State the blood parasite species.
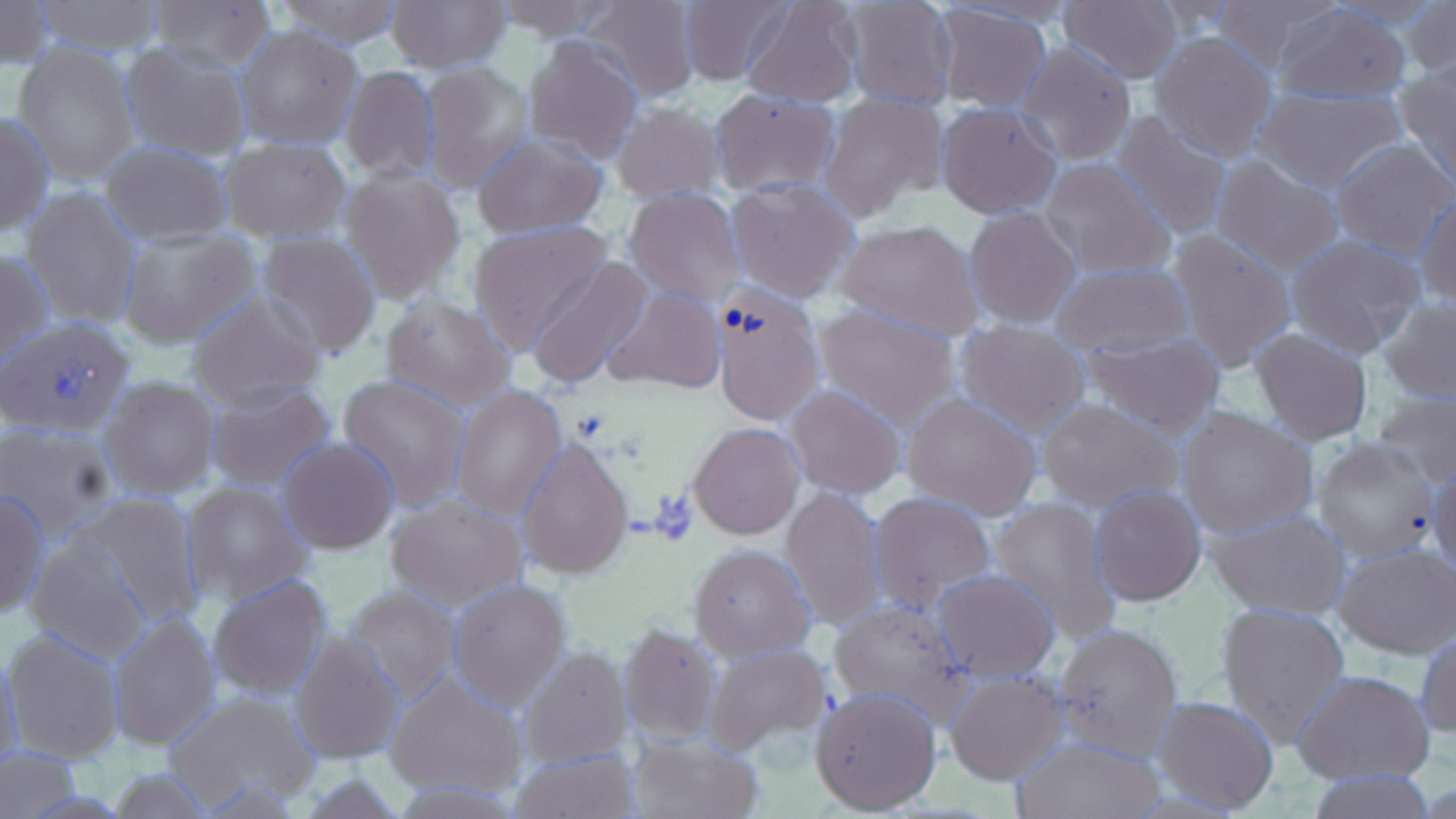
Plasmodium ovale.

Summary:
  - Coordinate format: approximate bounding boxes as named x1/y1/x2/y2 corners in pixels
  - Platelet locations: (x1=49, y1=357, x2=98, y2=403), (x1=649, y1=490, x2=699, y2=544)
  - Plasmodium ovale-infected red blood cell locations: (x1=710, y1=280, x2=825, y2=427)
  - Uninfected red blood cell locations: (x1=0, y1=0, x2=53, y2=71), (x1=32, y1=0, x2=166, y2=54), (x1=147, y1=0, x2=276, y2=71), (x1=271, y1=0, x2=408, y2=47), (x1=491, y1=0, x2=630, y2=42), (x1=680, y1=0, x2=798, y2=88), (x1=740, y1=0, x2=865, y2=108), (x1=840, y1=0, x2=958, y2=109), (x1=1058, y1=0, x2=1184, y2=83), (x1=1205, y1=0, x2=1347, y2=71), (x1=386, y1=1, x2=513, y2=73), (x1=578, y1=1, x2=697, y2=102), (x1=1405, y1=1, x2=1456, y2=89), (x1=931, y1=3, x2=1055, y2=115), (x1=1269, y1=3, x2=1412, y2=104), (x1=235, y1=25, x2=364, y2=149), (x1=1149, y1=32, x2=1277, y2=160), (x1=522, y1=36, x2=645, y2=163), (x1=120, y1=41, x2=252, y2=161), (x1=12, y1=42, x2=141, y2=187), (x1=1016, y1=42, x2=1135, y2=166), (x1=418, y1=62, x2=534, y2=191), (x1=1395, y1=62, x2=1456, y2=187), (x1=340, y1=65, x2=438, y2=182), (x1=1256, y1=84, x2=1404, y2=191), (x1=709, y1=87, x2=840, y2=197), (x1=821, y1=92, x2=946, y2=220), (x1=610, y1=102, x2=725, y2=202), (x1=937, y1=102, x2=1062, y2=218), (x1=0, y1=110, x2=53, y2=236), (x1=1113, y1=111, x2=1232, y2=238), (x1=470, y1=134, x2=608, y2=239), (x1=219, y1=136, x2=350, y2=242), (x1=1330, y1=139, x2=1456, y2=260), (x1=100, y1=143, x2=232, y2=244), (x1=1212, y1=155, x2=1345, y2=275), (x1=1039, y1=159, x2=1174, y2=278), (x1=341, y1=167, x2=467, y2=305), (x1=725, y1=177, x2=858, y2=301), (x1=21, y1=187, x2=142, y2=328), (x1=625, y1=187, x2=742, y2=307), (x1=1414, y1=196, x2=1456, y2=305), (x1=965, y1=206, x2=1081, y2=328), (x1=834, y1=219, x2=985, y2=340), (x1=468, y1=220, x2=614, y2=348), (x1=115, y1=227, x2=260, y2=349), (x1=1165, y1=228, x2=1298, y2=374), (x1=256, y1=232, x2=382, y2=357), (x1=1285, y1=233, x2=1425, y2=358), (x1=1, y1=248, x2=50, y2=373), (x1=529, y1=257, x2=654, y2=387), (x1=1052, y1=261, x2=1191, y2=358), (x1=603, y1=288, x2=724, y2=394), (x1=188, y1=291, x2=326, y2=410), (x1=380, y1=294, x2=515, y2=409), (x1=1376, y1=296, x2=1456, y2=404), (x1=812, y1=304, x2=960, y2=426), (x1=2, y1=317, x2=136, y2=438), (x1=956, y1=321, x2=1089, y2=434), (x1=1251, y1=327, x2=1374, y2=447), (x1=1081, y1=330, x2=1224, y2=438), (x1=338, y1=373, x2=471, y2=509), (x1=101, y1=376, x2=218, y2=498), (x1=205, y1=378, x2=337, y2=492), (x1=451, y1=384, x2=566, y2=522), (x1=787, y1=386, x2=906, y2=497), (x1=1370, y1=387, x2=1456, y2=489), (x1=901, y1=392, x2=1041, y2=521), (x1=1036, y1=399, x2=1184, y2=510), (x1=1174, y1=406, x2=1320, y2=537), (x1=0, y1=420, x2=117, y2=542), (x1=688, y1=423, x2=803, y2=539), (x1=1312, y1=437, x2=1438, y2=560), (x1=278, y1=438, x2=398, y2=552), (x1=516, y1=438, x2=635, y2=580), (x1=1428, y1=460, x2=1456, y2=580), (x1=181, y1=482, x2=312, y2=605), (x1=1090, y1=484, x2=1207, y2=606), (x1=0, y1=487, x2=48, y2=621), (x1=782, y1=488, x2=885, y2=629), (x1=68, y1=491, x2=205, y2=624), (x1=870, y1=491, x2=998, y2=614), (x1=386, y1=494, x2=526, y2=608), (x1=988, y1=494, x2=1123, y2=641), (x1=1205, y1=508, x2=1353, y2=620), (x1=26, y1=535, x2=148, y2=659), (x1=1334, y1=542, x2=1455, y2=659), (x1=689, y1=544, x2=815, y2=661), (x1=934, y1=571, x2=1061, y2=681), (x1=208, y1=573, x2=333, y2=701), (x1=448, y1=579, x2=571, y2=707), (x1=343, y1=583, x2=463, y2=707), (x1=829, y1=599, x2=973, y2=726), (x1=1216, y1=601, x2=1351, y2=744), (x1=107, y1=611, x2=220, y2=751), (x1=1053, y1=621, x2=1183, y2=760), (x1=620, y1=623, x2=719, y2=745), (x1=3, y1=626, x2=127, y2=763), (x1=1414, y1=628, x2=1456, y2=740), (x1=291, y1=629, x2=406, y2=762), (x1=703, y1=643, x2=831, y2=758), (x1=519, y1=647, x2=632, y2=767), (x1=0, y1=648, x2=23, y2=780), (x1=945, y1=669, x2=1066, y2=784), (x1=1294, y1=670, x2=1435, y2=785), (x1=386, y1=674, x2=526, y2=799), (x1=811, y1=684, x2=943, y2=816), (x1=167, y1=687, x2=316, y2=810), (x1=1152, y1=695, x2=1280, y2=814), (x1=627, y1=733, x2=764, y2=819), (x1=1010, y1=734, x2=1166, y2=819), (x1=508, y1=745, x2=637, y2=818), (x1=2, y1=747, x2=80, y2=817), (x1=106, y1=766, x2=219, y2=818), (x1=1297, y1=767, x2=1440, y2=818)
  - Field of view: single
  - Modality: optical microscopy
  - Magnification: 1000x
  - Preparation: thin blood film
  - Stain: May-Grünwald-Giemsa
  - Image size: 1456×819 pixels